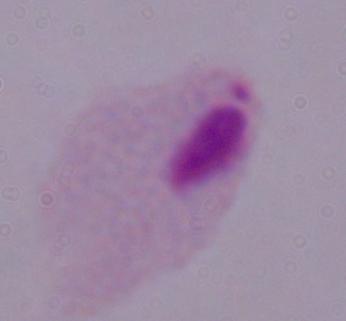

Summary:
  - Magnification: 1000x
  - Identification: trichomonad
  - Modality: photomicrograph